Locate every uninfected red blood cell.
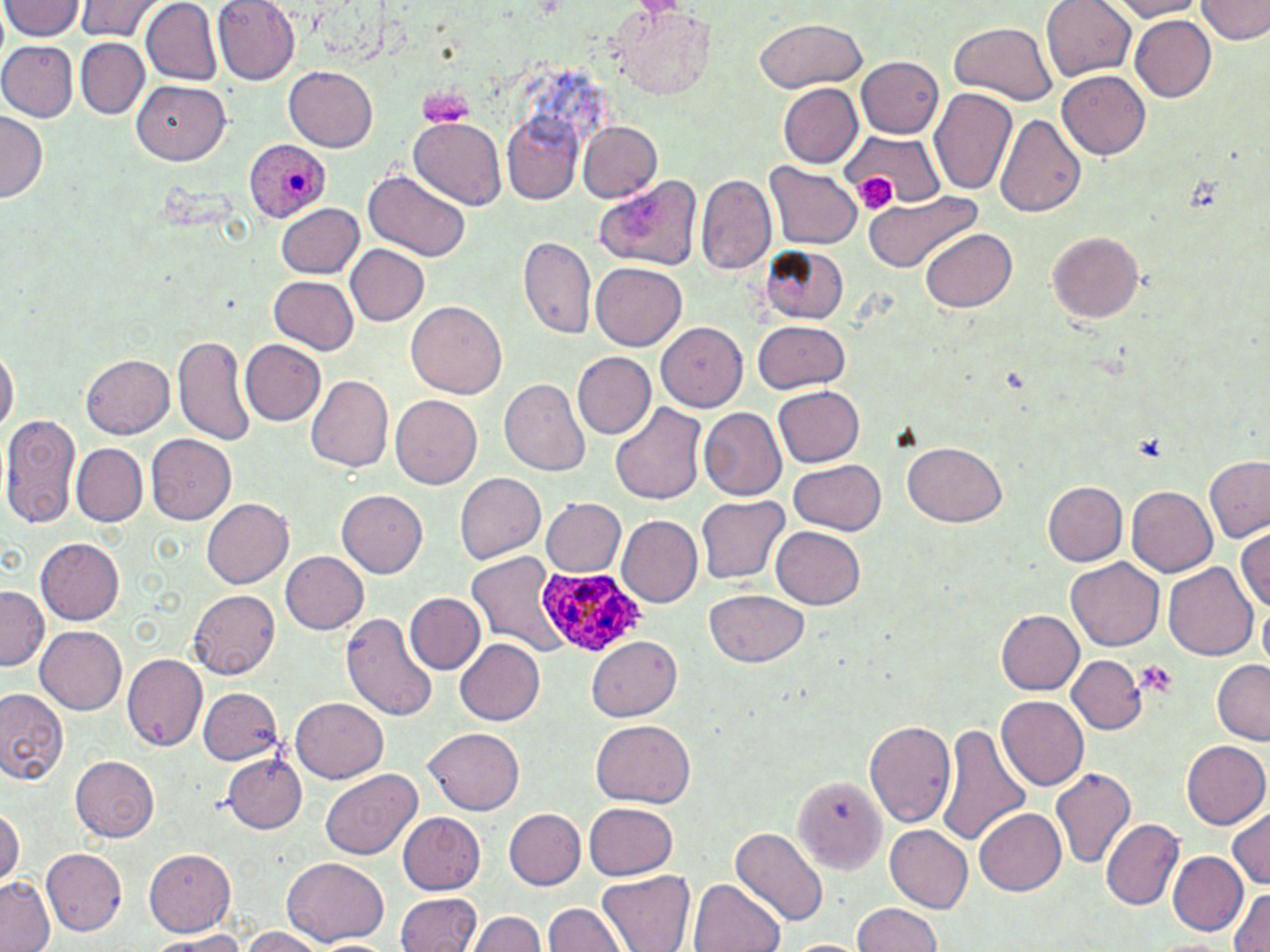

Approximate bounding boxes as (x1, y1, x2, y2) in pixels.
Uninfected red blood cells: (78, 0, 158, 41), (141, 0, 224, 87), (212, 0, 301, 85), (1042, 0, 1134, 82), (1104, 0, 1204, 21), (1199, 0, 1270, 44), (1, 2, 85, 43), (608, 6, 715, 99), (1128, 14, 1214, 101), (755, 18, 865, 91), (948, 21, 1058, 103), (75, 38, 146, 117), (0, 40, 78, 122), (856, 56, 944, 139), (283, 67, 377, 151), (1057, 70, 1151, 158), (131, 82, 230, 165), (777, 83, 861, 168), (932, 88, 1018, 196), (504, 111, 581, 202), (0, 112, 46, 206), (995, 114, 1086, 219), (409, 117, 506, 209), (579, 121, 662, 202), (842, 129, 942, 211), (764, 162, 861, 250), (362, 171, 472, 262), (591, 173, 701, 271), (698, 174, 774, 273), (863, 189, 982, 275), (278, 203, 365, 278), (918, 226, 1021, 312), (1048, 230, 1146, 324), (518, 237, 596, 341), (759, 244, 849, 320), (344, 245, 429, 326), (591, 262, 686, 352), (267, 275, 358, 354), (407, 302, 507, 399), (657, 320, 751, 411), (753, 321, 850, 394), (174, 333, 256, 448), (239, 340, 324, 425), (0, 342, 16, 446), (572, 352, 655, 439), (82, 354, 176, 438), (308, 375, 397, 471), (501, 378, 590, 476), (773, 384, 864, 466), (390, 395, 482, 489), (610, 402, 707, 506), (699, 408, 785, 498), (1, 414, 83, 532), (65, 429, 142, 596), (146, 434, 236, 526), (902, 441, 1007, 528), (71, 443, 145, 526), (1204, 457, 1270, 543), (789, 459, 885, 533), (453, 472, 546, 565), (1042, 479, 1127, 565), (1127, 485, 1218, 577), (336, 489, 427, 579), (696, 496, 787, 586), (201, 498, 294, 589), (540, 498, 624, 578), (616, 516, 701, 610), (1234, 525, 1269, 616), (771, 526, 866, 608), (37, 537, 125, 624), (280, 551, 368, 634), (465, 551, 568, 656), (1067, 559, 1164, 652), (1164, 562, 1257, 662), (0, 589, 46, 673), (188, 590, 280, 679), (705, 590, 810, 667), (405, 593, 486, 675), (342, 609, 437, 719), (995, 610, 1083, 695), (36, 628, 127, 713), (455, 636, 545, 723), (585, 636, 683, 720), (122, 654, 208, 751), (1066, 654, 1145, 734), (1212, 661, 1269, 744), (199, 687, 283, 766), (0, 689, 68, 786), (995, 697, 1088, 790), (290, 698, 388, 783), (591, 718, 695, 808), (866, 718, 957, 830), (936, 723, 1032, 846), (424, 727, 526, 814), (1184, 740, 1270, 830), (223, 755, 306, 833), (72, 757, 161, 841), (1050, 768, 1136, 871), (320, 770, 421, 861), (793, 773, 888, 874), (583, 800, 678, 878), (1225, 804, 1268, 891), (973, 808, 1066, 896), (505, 809, 585, 889), (0, 810, 23, 881), (398, 812, 486, 895), (1102, 819, 1185, 911), (884, 825, 973, 914), (730, 826, 829, 926), (144, 847, 234, 934), (43, 849, 126, 935), (1170, 851, 1246, 934), (280, 857, 391, 945), (597, 871, 692, 952), (0, 877, 54, 952), (690, 878, 784, 952), (1228, 886, 1270, 952), (393, 893, 480, 952), (851, 902, 946, 952), (543, 904, 625, 952), (471, 909, 543, 952), (238, 926, 336, 952), (141, 931, 259, 950), (1148, 934, 1237, 951), (785, 937, 865, 952).

Platelet locations: (416, 84, 475, 130), (858, 173, 890, 210), (1134, 661, 1176, 694). Plasmodium ovale-infected red blood cell locations: (245, 139, 330, 224), (536, 569, 645, 656). Slide-level diagnosis: Plasmodium ovale. Optical microscopy. Captured at 1000x magnification. May-Grünwald-Giemsa stain. Single field of view. Image is 1270×952 pixels. Thin blood film.